Assess this cell for malaria.
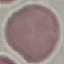

It is uninfected.

Giemsa-stained preparation. Thin blood film. Cell patch, automatically extracted from a larger field of view and resized to 64 × 64 pixels. Photographed with a smartphone camera at the microscope eyepiece.